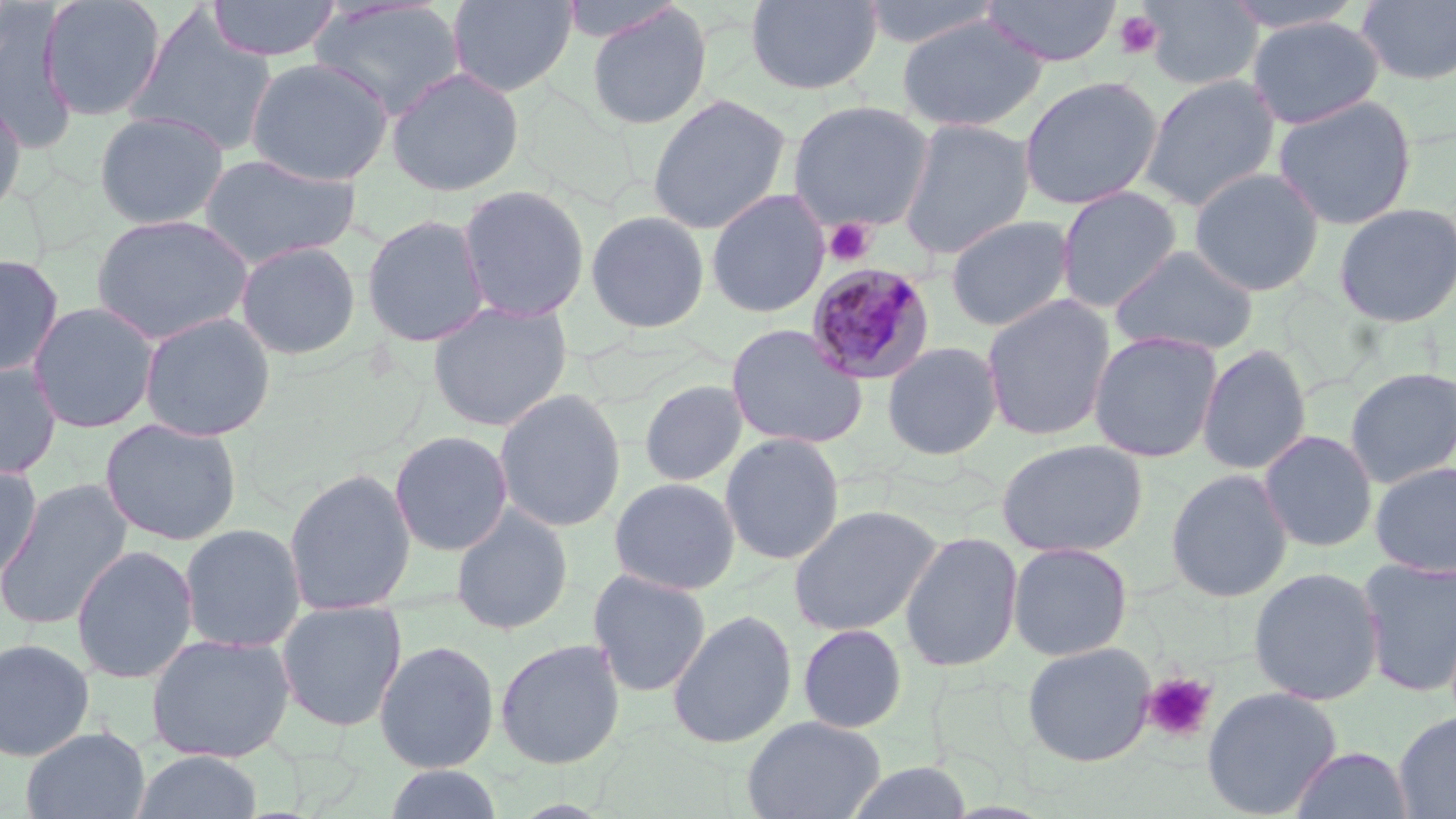

slide-level diagnosis = Plasmodium malariae
image size = 1456×819 pixels
field of view = single
stain = May-Grünwald-Giemsa
modality = optical microscopy
Plasmodium malariae-infected red blood cell locations = approximate bounding boxes as (x1, y1, x2, y2) in pixels: (805, 261, 937, 385)
preparation = thin blood smear
uninfected red blood cell locations = approximate bounding boxes as (x1, y1, x2, y2) in pixels: (38, 0, 167, 121), (206, 0, 341, 62), (447, 0, 577, 97), (556, 0, 685, 44), (746, 0, 882, 95), (857, 0, 1006, 50), (980, 0, 1123, 67), (1139, 0, 1263, 92), (1219, 0, 1370, 34), (1356, 0, 1456, 86), (308, 1, 466, 120), (585, 4, 713, 130), (1, 7, 75, 149), (126, 8, 278, 157), (896, 14, 1046, 133), (1247, 16, 1385, 129), (245, 57, 393, 186), (386, 67, 525, 197), (1138, 73, 1282, 211), (1018, 75, 1163, 211), (0, 92, 28, 221), (646, 93, 792, 235), (1271, 95, 1418, 230), (787, 99, 936, 231), (93, 110, 230, 229), (897, 117, 1035, 260), (197, 153, 361, 270), (1188, 167, 1326, 297), (456, 184, 591, 323), (1054, 185, 1183, 313), (706, 189, 830, 319), (1332, 202, 1456, 327), (585, 209, 711, 333), (90, 213, 254, 344), (361, 213, 491, 347), (945, 214, 1076, 332), (235, 239, 362, 360), (1109, 245, 1260, 357), (0, 253, 64, 378), (981, 294, 1117, 442), (27, 301, 161, 434), (427, 301, 573, 432), (138, 311, 276, 442), (725, 323, 868, 450), (1088, 331, 1224, 463), (881, 340, 1003, 461), (1196, 344, 1311, 476), (0, 361, 63, 480), (1343, 367, 1456, 488), (639, 379, 749, 487), (493, 388, 627, 532), (99, 417, 243, 546), (1258, 429, 1378, 553), (389, 430, 513, 556), (719, 432, 845, 566), (995, 438, 1148, 558), (1369, 460, 1456, 578), (0, 462, 42, 584), (283, 466, 416, 616), (1165, 468, 1293, 603), (608, 477, 741, 595), (0, 479, 134, 632), (788, 503, 943, 637), (450, 504, 573, 635), (179, 523, 306, 653), (900, 530, 1023, 673), (1007, 541, 1133, 661), (70, 544, 198, 684), (1356, 556, 1456, 697), (1247, 566, 1384, 706), (587, 568, 711, 697), (275, 601, 407, 732), (666, 609, 797, 749), (796, 623, 908, 734), (145, 633, 296, 763), (0, 638, 96, 762), (494, 638, 626, 770), (373, 640, 500, 773), (1021, 641, 1156, 767), (1201, 686, 1342, 818), (1393, 710, 1456, 818), (742, 715, 886, 819), (20, 726, 150, 819), (1289, 746, 1413, 819), (130, 749, 264, 819), (842, 762, 973, 819), (383, 765, 504, 819)
magnification = 1000x
platelet locations = approximate bounding boxes as (x1, y1, x2, y2) in pixels: (1113, 10, 1163, 59), (823, 218, 876, 267), (1142, 672, 1217, 744)